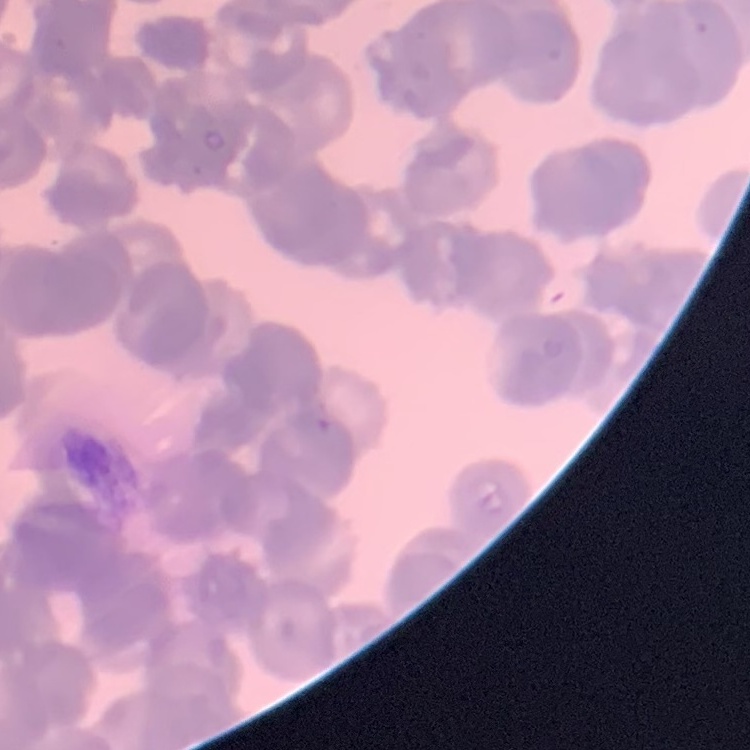

red_blood_cell_morphology: rouleaux formation
stain: Field's or Giemsa
image_type: square crop of a larger photomicrograph
preparation: thin blood film